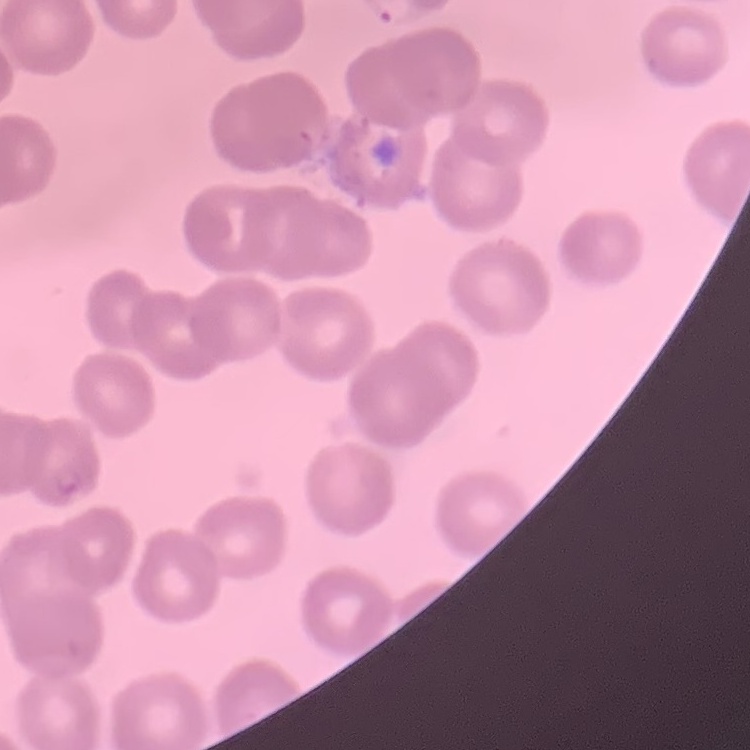
The erythrocytes show no rouleaux formation. One tile cut from a larger photomicrograph. Thin peripheral smear. Stained with either Field's or Giemsa.